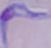

Summary:
  - Magnification: 1000x
  - Identification: trypanosome
  - Modality: micrograph